Identify the preparation type.
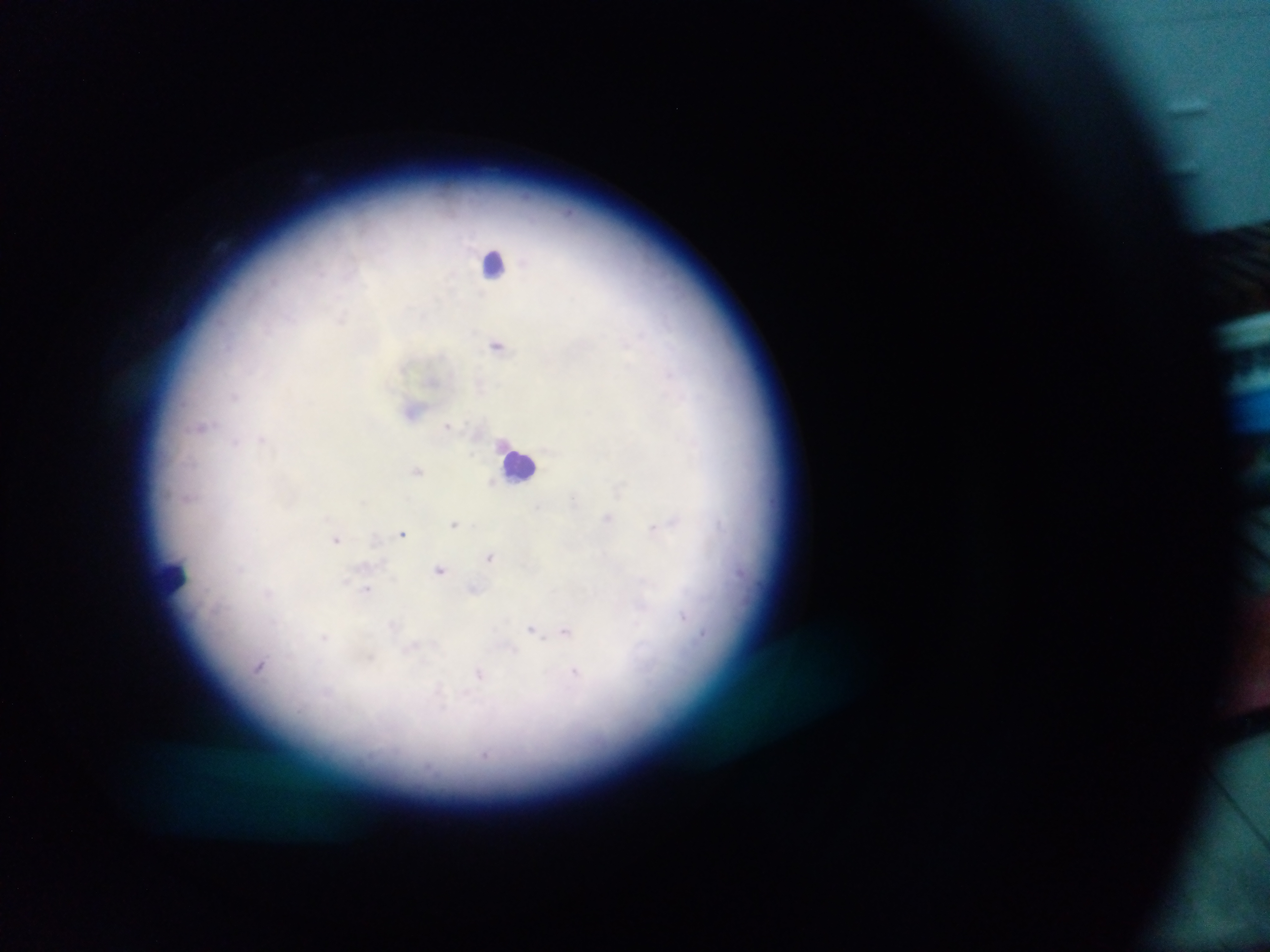

Thick blood film.

Approximate centers as x y in pixels.
Summary:
  - Malaria parasite locations: 341 318; 640 335; 627 342; 497 344; 669 373; 671 383; 235 396; 449 424; 204 427; 236 442; 263 442; 500 447; 694 450; 418 471; 492 480; 623 489; 574 500; 608 517; 675 522; 720 524; 454 525; 653 529; 403 534; 337 541; 490 557; 241 568; 440 571; 748 579; 366 591; 267 592; 685 616; 393 630; 567 631; 532 632; 702 633; 325 637; 367 657; 261 666; 577 677; 480 678; 441 697
  - Leukocyte locations: 498 261; 529 461; 175 575
  - Field of view: single
  - Image size: 1270×952 pixels
  - Capture: mobile-phone photograph through a microscope
  - Country: Ghana